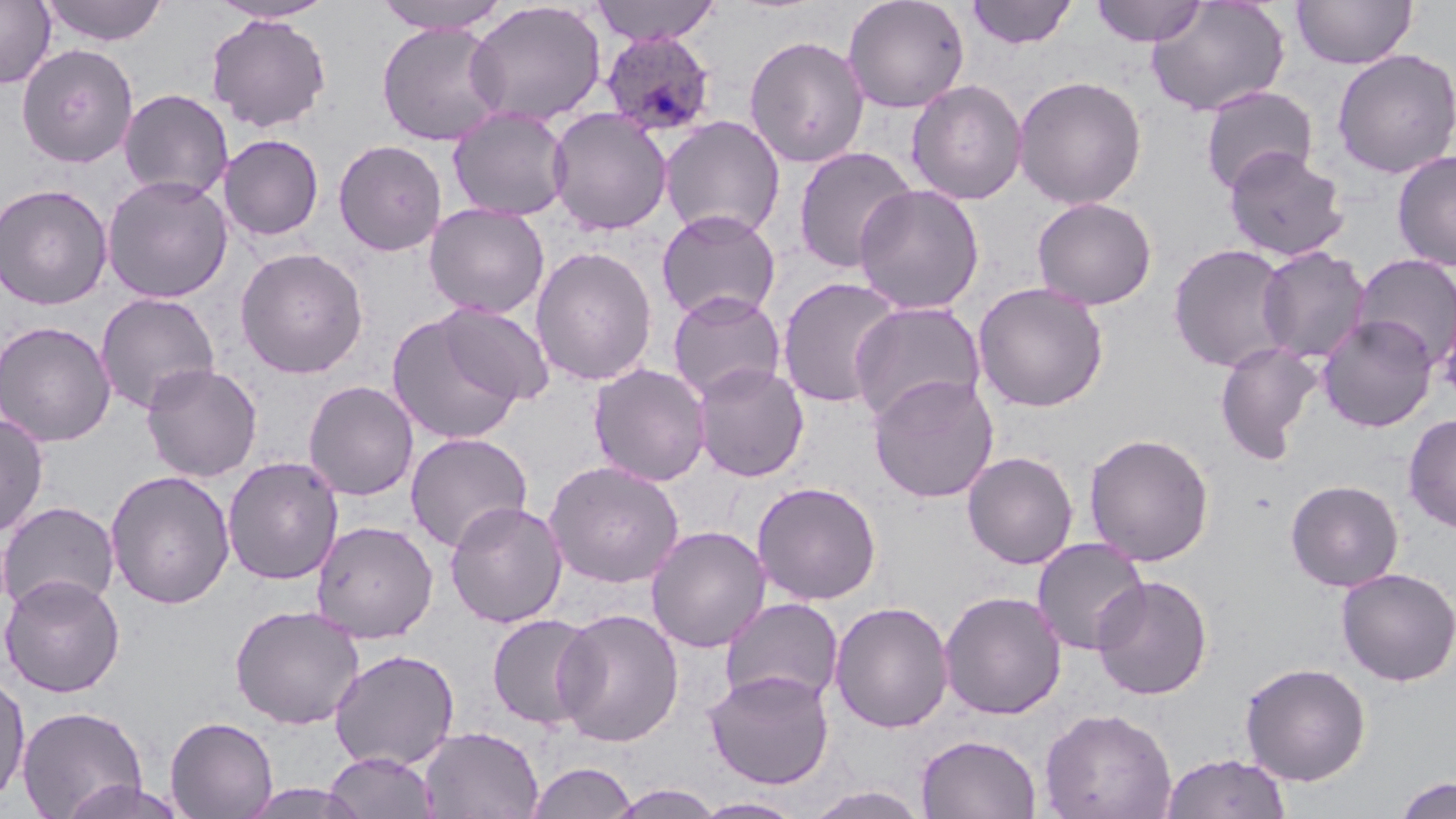

slide-level diagnosis = Plasmodium ovale
uninfected red blood cell locations = approximate bounding boxes as (x1,y1)-(x2,y2) corner pairs in pixels: (40,0)-(169,46), (372,0)-(510,33), (589,0)-(720,45), (842,0)-(969,113), (965,0)-(1077,49), (1091,0)-(1208,46), (1146,0)-(1289,117), (1291,0)-(1418,69), (0,1)-(55,88), (208,1)-(338,25), (465,1)-(607,127), (205,14)-(332,133), (376,22)-(507,146), (743,34)-(870,168), (16,43)-(138,168), (1331,49)-(1456,179), (1012,75)-(1148,210), (906,79)-(1028,205), (1199,85)-(1319,195), (118,88)-(234,201), (447,106)-(572,221), (548,108)-(673,235), (659,115)-(787,240), (218,134)-(324,240), (332,139)-(447,255), (792,146)-(918,273), (1223,146)-(1350,262), (1391,150)-(1456,270), (101,174)-(233,304), (0,183)-(113,310), (853,183)-(985,314), (1031,196)-(1157,310), (424,203)-(550,320), (655,209)-(781,323), (1167,243)-(1294,373), (531,246)-(658,386), (1256,246)-(1371,364), (234,247)-(369,379), (1352,254)-(1456,369), (776,276)-(905,408), (972,282)-(1109,413), (667,290)-(786,403), (95,293)-(220,414), (848,300)-(987,426), (436,302)-(555,406), (386,311)-(523,445), (1317,314)-(1438,432), (0,320)-(116,447), (1214,340)-(1323,463), (692,362)-(809,481), (140,363)-(263,482), (588,363)-(711,486), (867,373)-(999,504), (302,380)-(419,501), (0,413)-(49,537), (1403,413)-(1456,532), (405,432)-(532,552), (1083,432)-(1215,566), (962,451)-(1079,569), (222,456)-(344,585), (544,459)-(685,588), (105,470)-(236,609), (1285,478)-(1404,592), (751,481)-(882,605), (444,500)-(567,628), (0,501)-(120,614), (310,520)-(439,643), (646,525)-(771,653), (1031,537)-(1150,655), (1335,567)-(1456,687), (1,574)-(126,698), (1092,574)-(1213,701), (938,590)-(1067,720), (719,597)-(843,708), (829,601)-(954,733), (229,604)-(366,729), (552,608)-(685,747), (486,613)-(599,731), (328,648)-(460,770), (1239,661)-(1372,785), (703,670)-(835,790), (0,671)-(30,806), (16,704)-(148,818), (1039,707)-(1177,819), (165,716)-(279,818), (419,726)-(544,819), (915,734)-(1042,819), (323,751)-(439,819), (1161,751)-(1293,819), (527,761)-(638,819), (1393,775)-(1455,818), (57,779)-(190,819), (236,784)-(369,819), (607,784)-(726,818), (804,785)-(932,819), (692,797)-(807,818)
image size = 1456×819 pixels
Plasmodium ovale-infected red blood cell locations = approximate bounding boxes as (x1,y1)-(x2,y2) corner pairs in pixels: (600,30)-(717,139)
preparation = thin blood smear
modality = light microscopy
stain = May-Grünwald-Giemsa
field of view = single
magnification = 1000x